Classify this cell by malaria status.
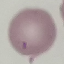
Uninfected.

Summary:
  - Preparation: thin blood smear
  - Stain: Giemsa
  - Image type: automatically extracted cell patch, resized to 64 × 64 pixels
  - Capture: smartphone camera at the microscope eyepiece